Locate every blood parasite and identify its species.
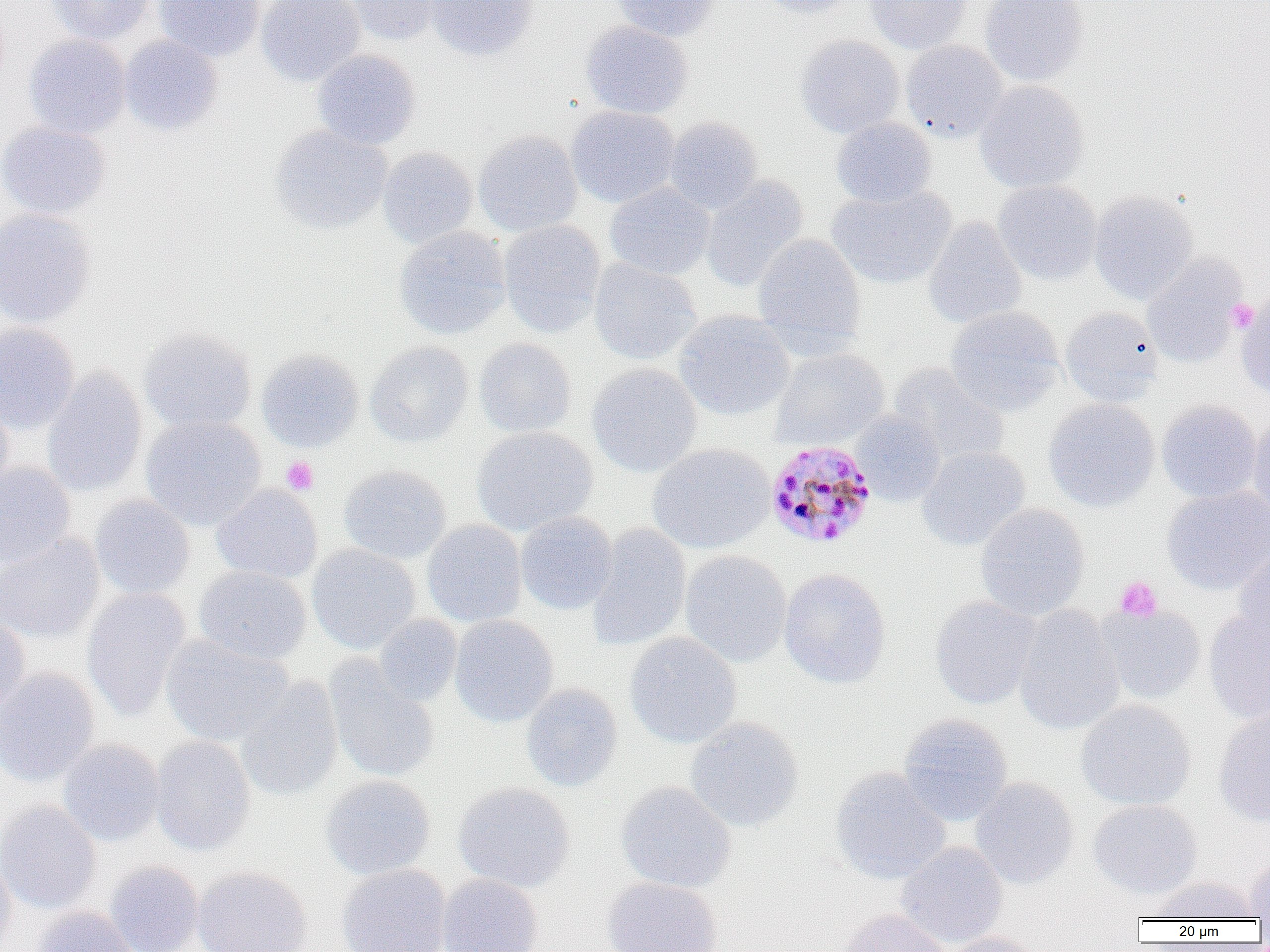

Approximate bounding boxes as [x1, y1, x2, y2] in pixels.
Plasmodium malariae-infected red blood cells: [765, 439, 878, 549].
No Plasmodium falciparum, Plasmodium ovale, Plasmodium vivax, Babesia divergens, or Trypanosoma brucei observed.

slide-level diagnosis = Plasmodium malariae
image size = 1270×952 pixels
uninfected red blood cell locations = approximate bounding boxes as [x1, y1, x2, y2] in pixels: [47, 0, 155, 45], [153, 0, 265, 61], [256, 0, 365, 86], [343, 0, 444, 46], [426, 0, 538, 60], [610, 0, 718, 41], [756, 0, 858, 19], [865, 0, 970, 54], [980, 0, 1088, 86], [580, 20, 693, 119], [24, 34, 131, 139], [794, 34, 905, 138], [119, 35, 223, 135], [901, 40, 1007, 142], [312, 49, 421, 149], [975, 81, 1088, 193], [566, 106, 679, 208], [664, 116, 764, 215], [831, 118, 936, 208], [0, 121, 111, 219], [269, 125, 392, 234], [473, 130, 583, 237], [377, 147, 478, 248], [700, 176, 808, 293], [993, 180, 1101, 285], [605, 182, 715, 281], [828, 185, 955, 287], [1089, 189, 1198, 305], [0, 208, 96, 327], [922, 216, 1027, 329], [498, 219, 606, 337], [393, 225, 511, 340], [752, 233, 866, 352], [1142, 256, 1245, 367], [589, 259, 701, 366], [1237, 294, 1270, 396], [945, 306, 1065, 417], [1060, 307, 1164, 406], [674, 310, 795, 421], [0, 322, 79, 433], [139, 327, 257, 434], [474, 338, 576, 438], [365, 341, 474, 448], [770, 347, 890, 451], [257, 348, 364, 452], [587, 363, 703, 477], [888, 363, 1008, 465], [42, 367, 148, 497], [1043, 398, 1159, 512], [0, 400, 14, 503], [1157, 400, 1262, 503], [850, 411, 946, 507], [140, 416, 267, 530], [1248, 417, 1270, 525], [471, 426, 597, 536], [647, 443, 775, 554], [916, 446, 1030, 552], [0, 462, 75, 568], [338, 464, 451, 563], [211, 483, 323, 583], [1162, 485, 1270, 595], [89, 495, 195, 600], [975, 503, 1090, 619], [515, 511, 618, 615], [422, 519, 527, 627], [587, 524, 691, 652], [0, 532, 104, 644], [307, 544, 421, 654], [1233, 547, 1270, 649], [680, 550, 792, 667], [194, 565, 311, 665], [779, 568, 891, 689], [82, 588, 191, 720], [929, 596, 1040, 710], [1013, 604, 1125, 736], [1098, 605, 1207, 704], [1203, 611, 1270, 724], [0, 612, 31, 727], [374, 614, 462, 706], [450, 615, 558, 727], [624, 632, 742, 748], [161, 634, 293, 745], [324, 658, 440, 784], [0, 667, 100, 786], [236, 677, 343, 802], [520, 684, 623, 792], [1075, 699, 1196, 810], [1214, 709, 1270, 827], [898, 713, 1013, 826], [685, 717, 804, 832], [150, 735, 256, 856], [57, 739, 165, 845], [829, 767, 951, 884], [320, 774, 436, 880], [970, 777, 1079, 889], [616, 781, 736, 893], [453, 782, 575, 893], [1088, 799, 1202, 899], [0, 801, 101, 914], [895, 842, 1008, 949], [0, 848, 16, 952], [1243, 855, 1270, 921], [105, 861, 205, 952], [337, 863, 451, 952], [192, 865, 312, 952], [437, 874, 543, 952], [601, 876, 723, 952], [1145, 876, 1258, 921], [32, 906, 139, 952], [839, 908, 950, 952], [941, 932, 1049, 952]
field of view = single
modality = optical microscopy
magnification = 1000x
platelet locations = approximate bounding boxes as [x1, y1, x2, y2] in pixels: [1225, 299, 1259, 333], [281, 456, 319, 495], [1115, 576, 1163, 622]
preparation = thin blood smear